Give the extent of all Plasmodium malariae-infected red blood cells.
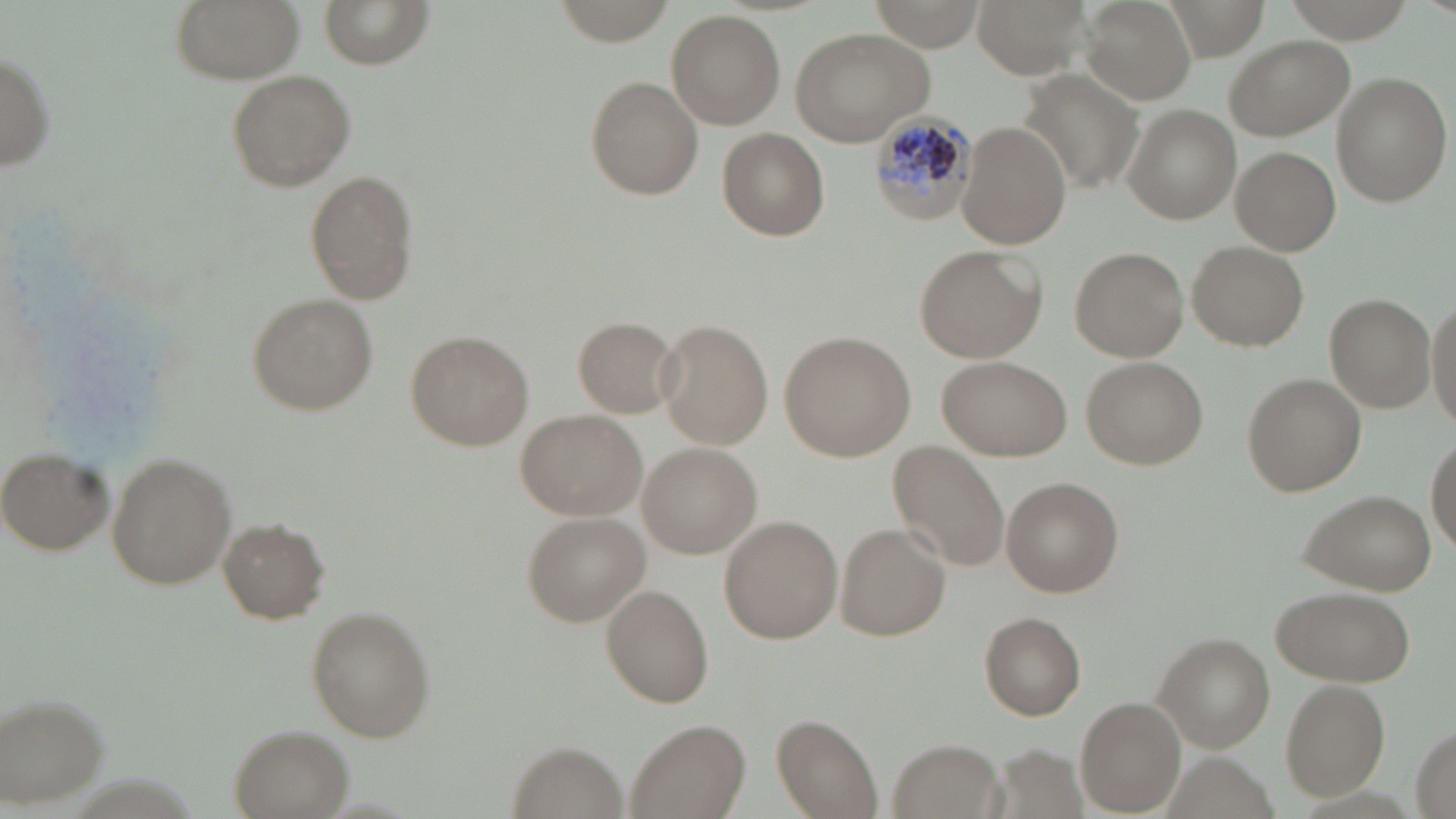

Approximate bounding boxes as [x1, y1, x2, y2] in pixels.
Plasmodium malariae-infected red blood cells: [869, 108, 977, 225].

Summary:
  - Uninfected red blood cell locations: [171, 0, 303, 84], [322, 0, 431, 68], [554, 0, 674, 45], [866, 0, 985, 53], [975, 0, 1091, 77], [1081, 0, 1195, 105], [1282, 0, 1416, 40], [667, 10, 785, 130], [790, 26, 936, 146], [1224, 35, 1353, 141], [0, 48, 56, 172], [1015, 67, 1143, 193], [226, 69, 356, 192], [1330, 72, 1452, 209], [585, 77, 702, 201], [1125, 106, 1239, 224], [956, 120, 1069, 249], [717, 128, 829, 239], [1231, 147, 1339, 256], [306, 172, 419, 305], [1188, 242, 1307, 351], [913, 244, 1046, 362], [1070, 245, 1190, 361], [1424, 289, 1456, 436], [246, 293, 377, 413], [1325, 293, 1435, 414], [572, 316, 679, 418], [656, 320, 773, 449], [781, 330, 916, 461], [406, 331, 533, 449], [938, 356, 1071, 461], [1081, 357, 1207, 470], [1242, 373, 1365, 496], [516, 408, 647, 521], [1428, 434, 1456, 550], [638, 442, 762, 560], [889, 442, 1011, 574], [1, 451, 113, 555], [105, 456, 236, 590], [1001, 477, 1124, 599], [1299, 491, 1438, 591], [521, 512, 650, 624], [719, 515, 841, 643], [219, 518, 327, 623], [835, 522, 950, 639], [601, 585, 715, 708], [1272, 585, 1416, 689], [306, 609, 433, 742], [979, 612, 1086, 720], [1152, 632, 1276, 752], [1281, 678, 1390, 802], [0, 694, 110, 810], [1076, 699, 1184, 815], [773, 713, 884, 817], [625, 719, 748, 819], [1413, 724, 1454, 818], [231, 725, 351, 817], [886, 738, 1007, 819], [511, 742, 622, 819]
  - Slide-level diagnosis: Plasmodium malariae
  - Image size: 1456×819 pixels
  - Magnification: 1000x
  - Field of view: single
  - Preparation: thin blood film
  - Modality: light microscopy
  - Stain: May-Grünwald-Giemsa